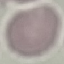

malaria status = uninfected
image type = cell patch, automatically extracted from a larger field of view and resized to 64 × 64 pixels
capture = smartphone camera at the microscope eyepiece
preparation = thin smear
stain = Giemsa